Assess the morphology of the erythrocytes.
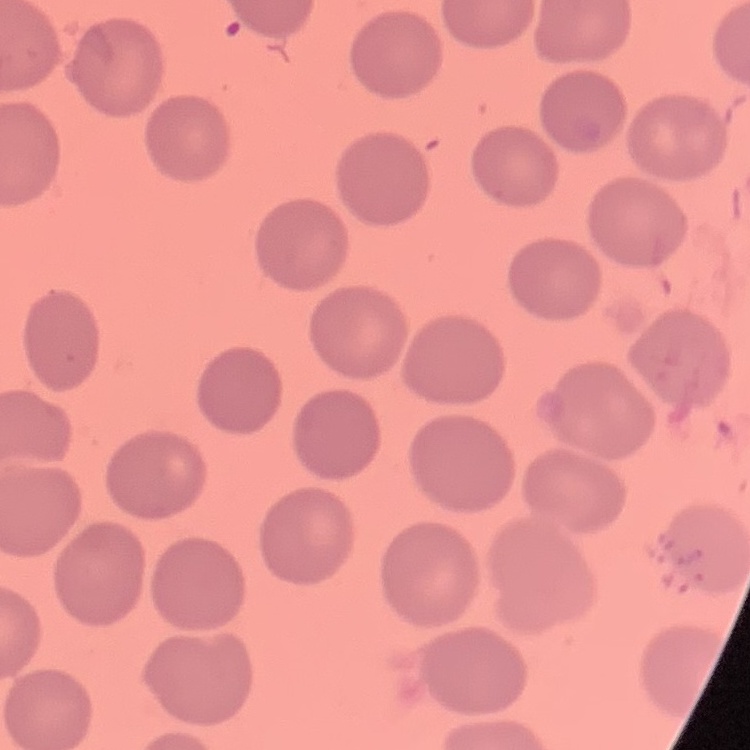

They show no rouleaux formation.

preparation = thin peripheral smear
image type = one tile cut from a larger photomicrograph
stain = Field's or Giemsa